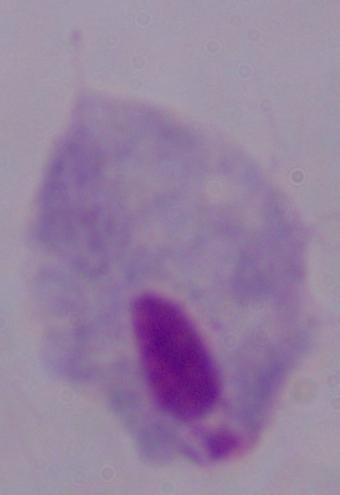

Micrograph. 1000x magnification. A trichomonad is shown.